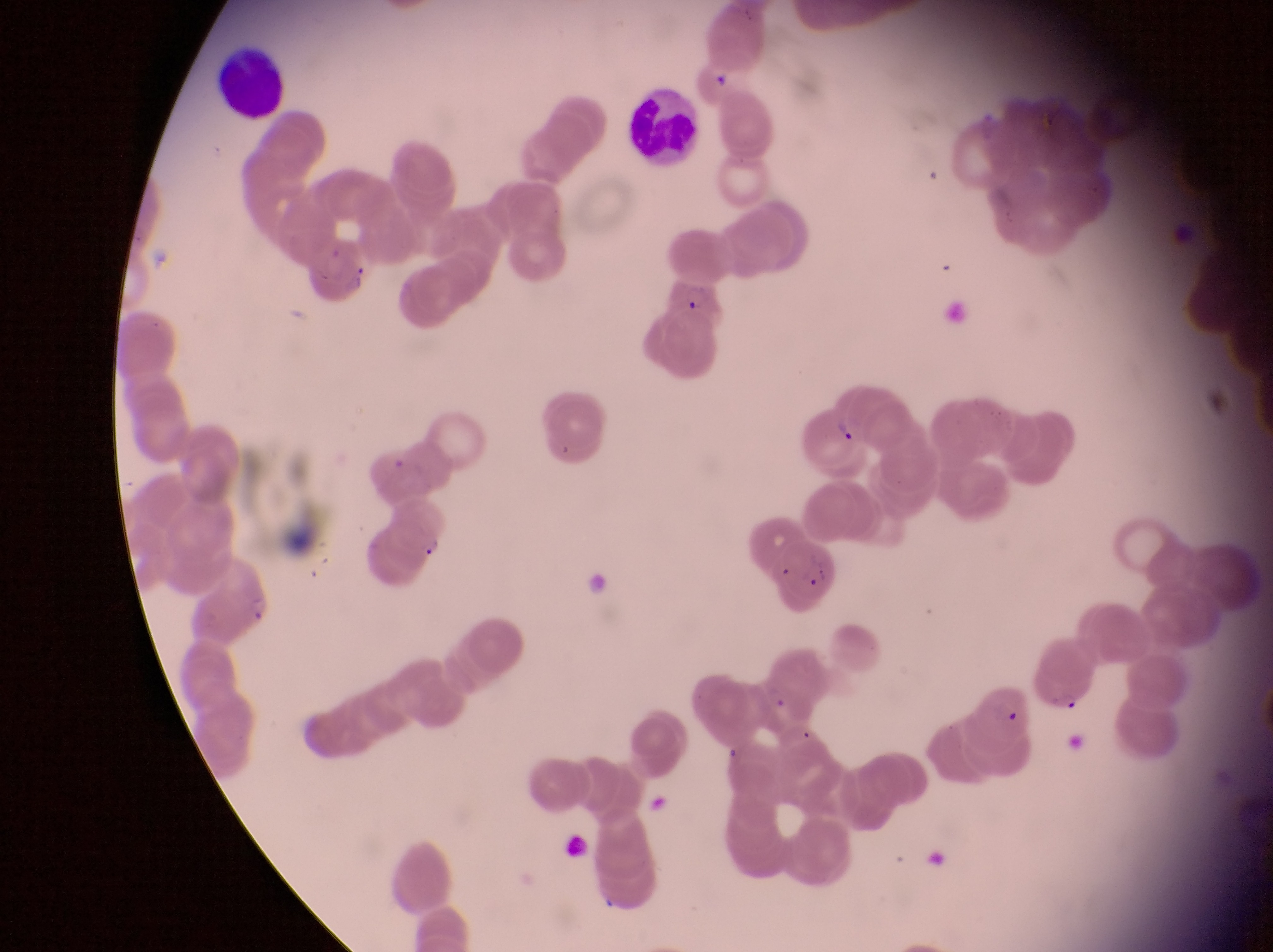

Approximate bounding boxes as {left, top, right, bottom} in pixels.
Summary:
  - Parasitised red blood cell locations: {664, 270, 726, 328}, {194, 558, 274, 637}, {1026, 645, 1095, 714}
  - Leukocyte locations: {210, 45, 289, 123}, {628, 85, 699, 168}
  - Field of view: single
  - Magnification: 1000x
  - Image size: 1273×952 pixels
  - Preparation: thin blood smear
  - Country: Uganda
  - Capture: smartphone photograph through the eyepiece of an Olympus CX-23 microscope